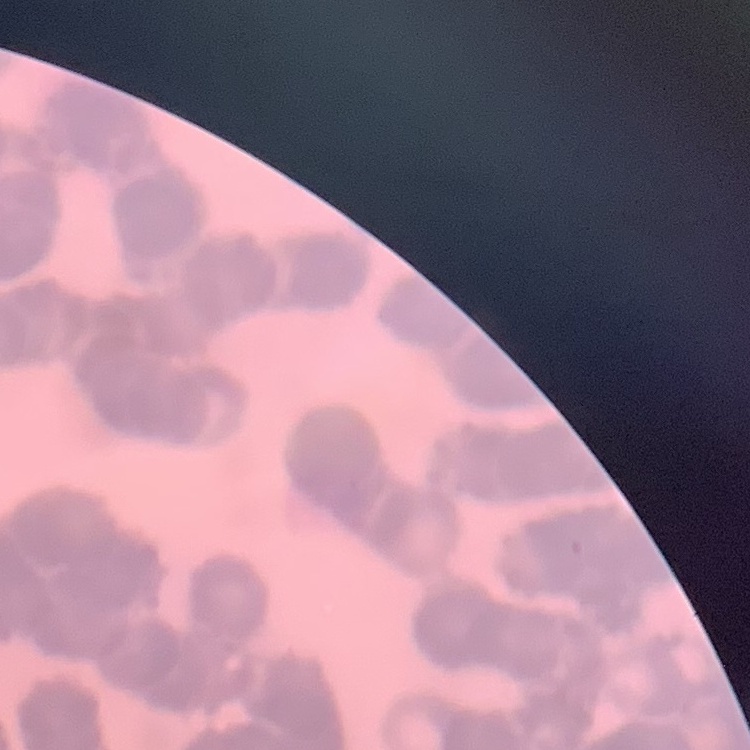 The red blood cells exhibit rouleaux formation. One tile cut from a larger photomicrograph. Field's or Giemsa stain. Thin peripheral smear.